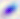
Toxoplasma gondii is shown. Captured at 400x magnification. Micrograph.